Classify this cell by malaria status.
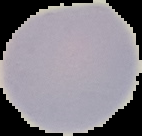

Uninfected.

preparation = thin blood smear
image type = segmented cell region on a black background
image size = 142×136 pixels